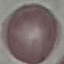
Summary:
  - Malaria status: uninfected
  - Capture: smartphone camera at the microscope eyepiece
  - Preparation: thin blood smear
  - Image type: cell patch, automatically extracted from a larger field of view and resized to 64 × 64 pixels
  - Stain: Giemsa